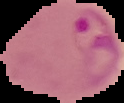 From a thin blood smear. Malaria status: parasitized. Image is 124×103 pixels. Segmented cell region on a black background.